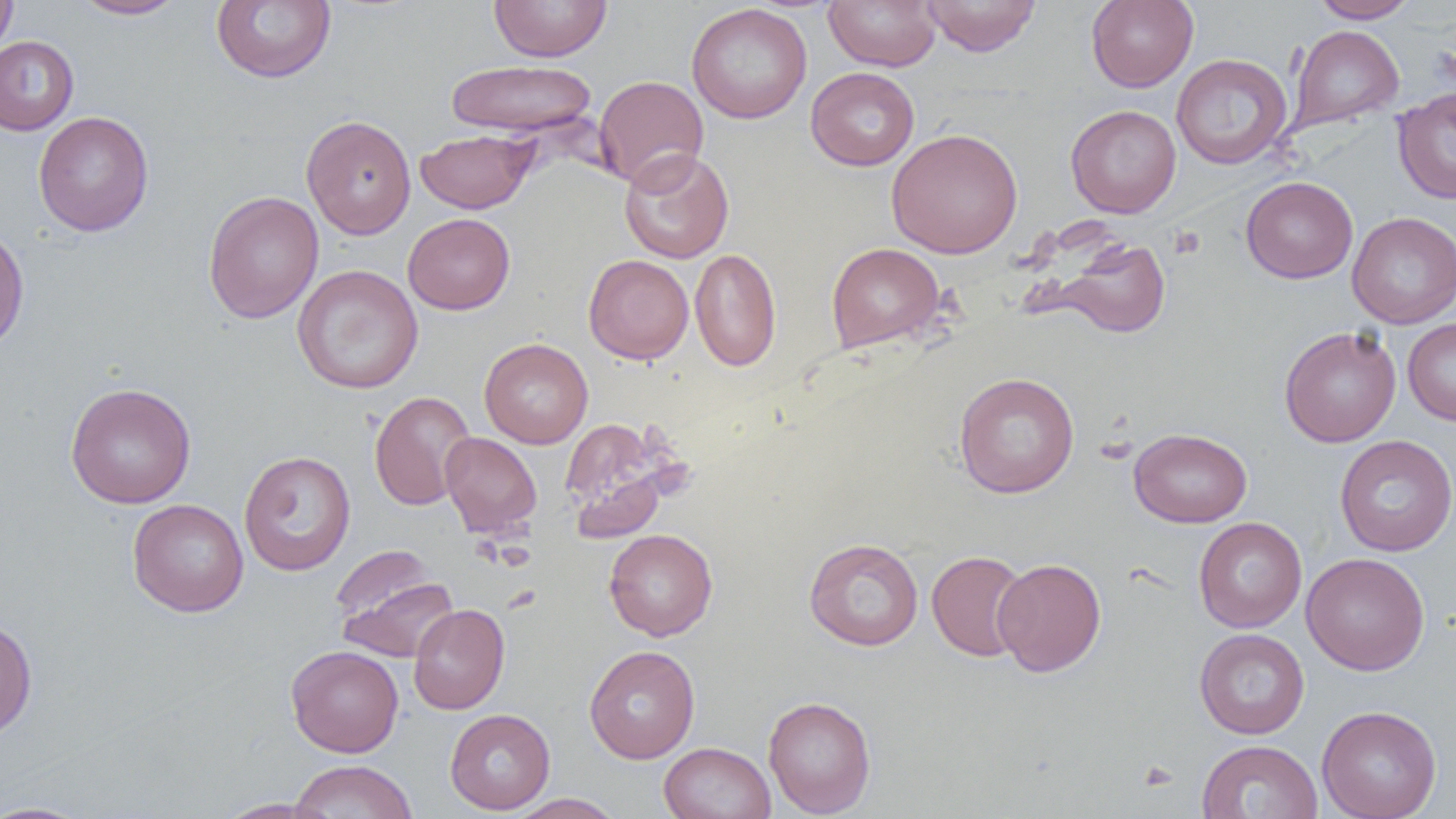

Summary:
  - Coordinate format: approximate bounding boxes as named x1/y1/x2/y2 corners in pixels
  - Uninfected red blood cell locations: (x1=0, y1=0, x2=17, y2=56), (x1=73, y1=0, x2=187, y2=19), (x1=211, y1=0, x2=336, y2=84), (x1=488, y1=0, x2=613, y2=62), (x1=824, y1=0, x2=941, y2=71), (x1=920, y1=0, x2=1041, y2=56), (x1=1086, y1=0, x2=1198, y2=92), (x1=1310, y1=0, x2=1418, y2=23), (x1=686, y1=3, x2=812, y2=124), (x1=1288, y1=24, x2=1404, y2=132), (x1=0, y1=36, x2=79, y2=135), (x1=1171, y1=53, x2=1292, y2=169), (x1=446, y1=59, x2=597, y2=138), (x1=806, y1=67, x2=919, y2=171), (x1=594, y1=75, x2=709, y2=190), (x1=1392, y1=86, x2=1456, y2=204), (x1=1065, y1=104, x2=1181, y2=218), (x1=33, y1=111, x2=154, y2=236), (x1=300, y1=114, x2=416, y2=240), (x1=416, y1=128, x2=539, y2=213), (x1=886, y1=128, x2=1023, y2=259), (x1=619, y1=149, x2=734, y2=264), (x1=1241, y1=176, x2=1358, y2=283), (x1=203, y1=190, x2=324, y2=323), (x1=1346, y1=211, x2=1456, y2=328), (x1=403, y1=213, x2=515, y2=315), (x1=0, y1=225, x2=29, y2=355), (x1=1049, y1=236, x2=1171, y2=339), (x1=826, y1=243, x2=944, y2=352), (x1=690, y1=248, x2=782, y2=372), (x1=583, y1=254, x2=694, y2=364), (x1=292, y1=264, x2=424, y2=394), (x1=1402, y1=318, x2=1456, y2=426), (x1=1279, y1=326, x2=1401, y2=447), (x1=479, y1=337, x2=593, y2=448), (x1=954, y1=372, x2=1079, y2=498), (x1=65, y1=382, x2=196, y2=508), (x1=369, y1=391, x2=476, y2=510), (x1=559, y1=418, x2=675, y2=536), (x1=1129, y1=428, x2=1253, y2=527), (x1=440, y1=432, x2=542, y2=537), (x1=1335, y1=435, x2=1456, y2=556), (x1=239, y1=450, x2=356, y2=577), (x1=127, y1=499, x2=248, y2=617), (x1=1193, y1=517, x2=1307, y2=633), (x1=604, y1=528, x2=718, y2=641), (x1=804, y1=537, x2=923, y2=650), (x1=329, y1=545, x2=437, y2=629), (x1=926, y1=550, x2=1031, y2=662), (x1=1301, y1=552, x2=1429, y2=675), (x1=993, y1=558, x2=1106, y2=676), (x1=334, y1=572, x2=459, y2=663), (x1=408, y1=604, x2=510, y2=714), (x1=0, y1=617, x2=37, y2=741), (x1=1194, y1=627, x2=1310, y2=739), (x1=286, y1=645, x2=404, y2=757), (x1=584, y1=645, x2=700, y2=763), (x1=763, y1=695, x2=877, y2=817), (x1=1317, y1=705, x2=1442, y2=819), (x1=445, y1=709, x2=555, y2=814), (x1=1195, y1=739, x2=1323, y2=819), (x1=659, y1=741, x2=776, y2=819), (x1=288, y1=759, x2=417, y2=819), (x1=506, y1=793, x2=626, y2=818), (x1=215, y1=798, x2=330, y2=818), (x1=0, y1=801, x2=94, y2=819)
  - Platelet locations: (x1=1138, y1=761, x2=1179, y2=792)
  - Slide-level diagnosis: negative for blood parasites
  - Field of view: single
  - Preparation: thin blood smear
  - Modality: light microscopy
  - Image size: 1456×819 pixels
  - Magnification: 1000x